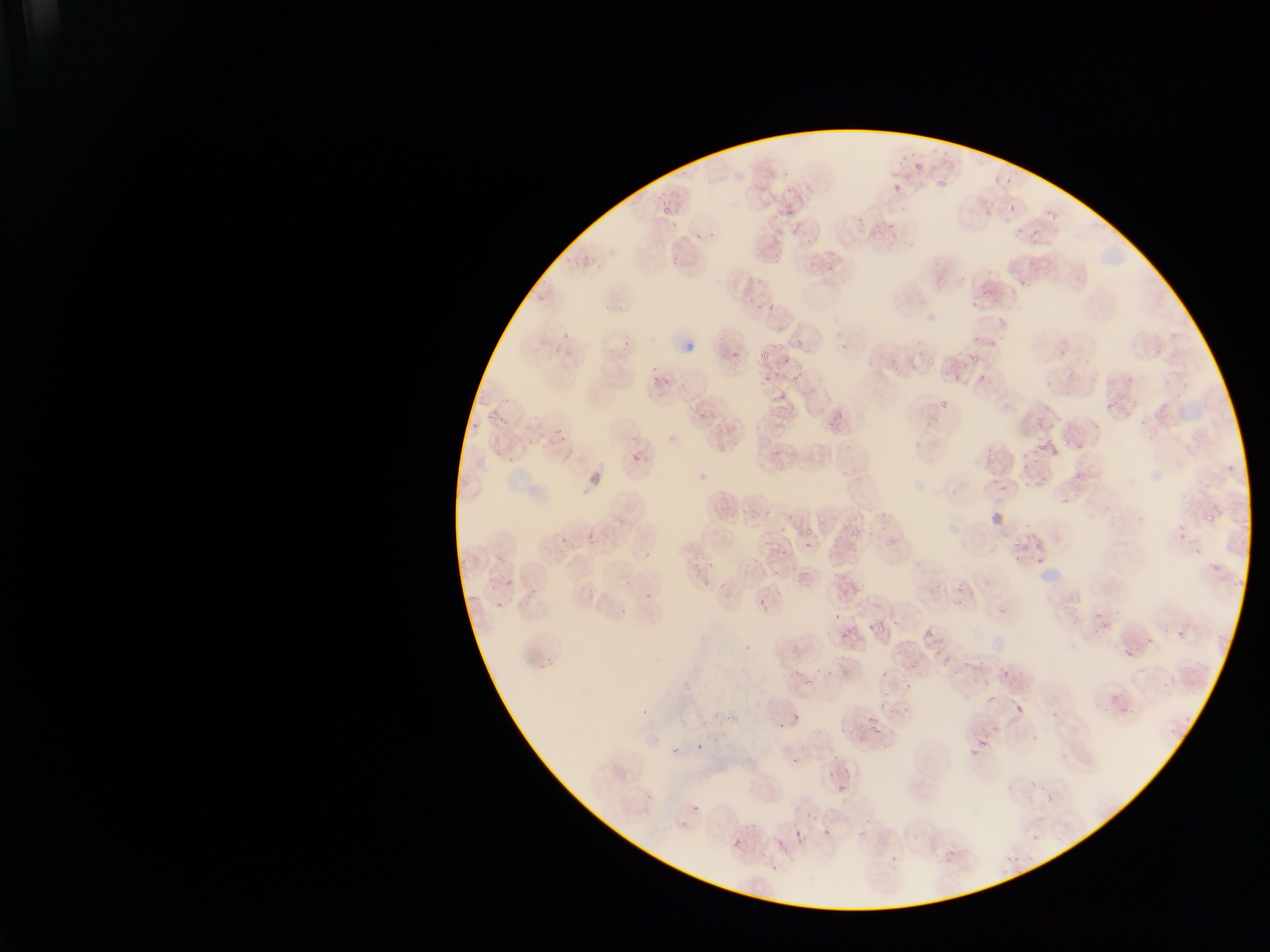
malaria parasite locations = approximate bounding boxes as {left, top, right, bottom} in pixels: {915, 154, 927, 171}, {892, 182, 903, 198}, {663, 206, 672, 216}, {761, 285, 779, 310}, {758, 347, 766, 360}, {778, 353, 787, 365}, {963, 354, 980, 371}, {787, 366, 804, 388}, {974, 372, 986, 383}, {649, 383, 657, 394}, {771, 383, 783, 399}, {1106, 391, 1127, 410}, {1156, 400, 1168, 412}, {935, 402, 954, 419}, {492, 415, 500, 425}, {714, 436, 726, 451}, {1037, 439, 1058, 458}, {1023, 461, 1030, 470}, {1071, 468, 1083, 483}, {1029, 472, 1051, 489}, {998, 481, 1009, 498}, {854, 511, 864, 525}, {1204, 514, 1216, 524}, {854, 521, 863, 542}, {1174, 521, 1185, 539}, {799, 527, 813, 538}, {557, 534, 570, 545}, {773, 536, 785, 552}, {1008, 538, 1024, 551}, {805, 539, 812, 550}, {1036, 556, 1044, 564}, {1210, 563, 1222, 570}, {789, 569, 805, 584}, {838, 571, 847, 583}, {698, 576, 710, 588}, {761, 593, 774, 614}, {872, 593, 884, 607}, {834, 610, 842, 617}, {1096, 610, 1104, 621}, {875, 619, 890, 636}, {924, 622, 935, 633}, {840, 625, 848, 638}, {1177, 630, 1188, 640}, {1145, 636, 1155, 646}, {919, 638, 930, 650}, {1127, 648, 1139, 663}, {960, 661, 971, 670}, {879, 665, 887, 677}, {801, 671, 812, 682}, {903, 679, 912, 688}, {1051, 703, 1063, 717}, {782, 704, 809, 725}, {1013, 705, 1023, 718}, {867, 714, 878, 722}, {852, 721, 860, 733}, {866, 723, 879, 740}, {977, 742, 986, 751}, {837, 776, 855, 793}, {691, 805, 699, 813}, {823, 822, 835, 835}, {794, 829, 804, 841}, {943, 835, 965, 870}, {732, 838, 742, 848}, {776, 840, 785, 849}, {770, 866, 777, 874} | approximate {x, y} pixel centers of objects too small to bound: {994, 698}
preparation = thin blood smear
image size = 1270×952 pixels
country = Ghana
capture = mobile-phone photograph through a microscope
field of view = single